Report the malaria status of this cell.
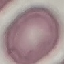
Uninfected.

{
  "capture": "smartphone through the microscope eyepiece",
  "stain": "Giemsa",
  "image_type": "automatically extracted cell patch, resized to 64 × 64 pixels",
  "preparation": "thin blood smear"
}